Give the extent of all uninfected red blood cells.
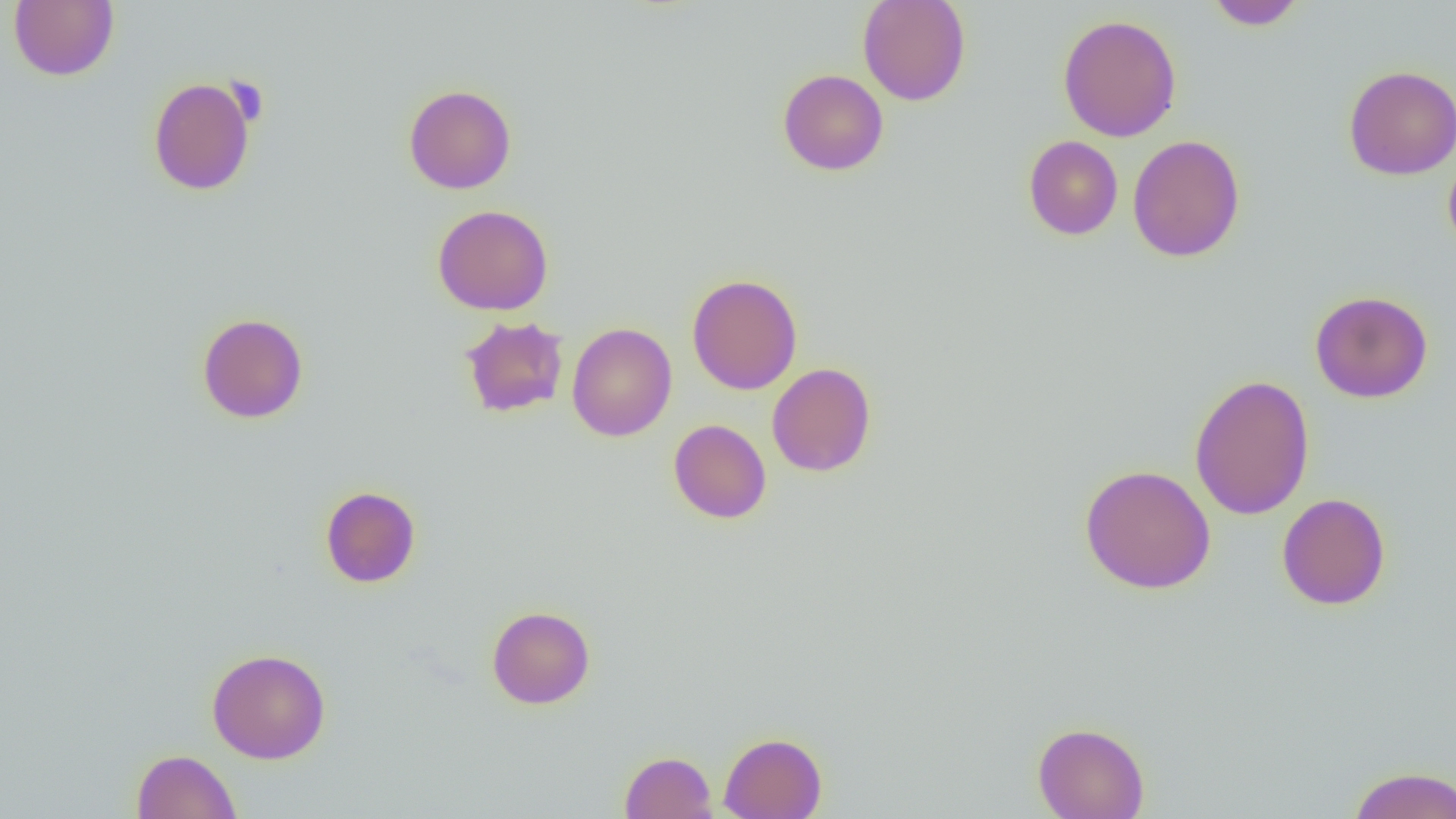
Approximate bounding boxes as (x1, y1, x2, y2) in pixels.
Uninfected red blood cells: (8, 0, 119, 81), (857, 0, 971, 106), (1206, 1, 1306, 30), (1058, 13, 1182, 142), (1342, 65, 1456, 180), (777, 69, 889, 175), (148, 76, 257, 196), (403, 84, 517, 194), (1023, 135, 1123, 240), (1127, 135, 1245, 262), (1443, 150, 1456, 257), (432, 204, 554, 316), (687, 273, 802, 395), (1309, 290, 1433, 404), (197, 313, 308, 423), (460, 316, 569, 418), (566, 322, 677, 442), (767, 363, 877, 477), (1189, 373, 1315, 521), (668, 419, 772, 523), (1079, 464, 1216, 594), (320, 485, 421, 588), (1277, 493, 1390, 610), (486, 605, 595, 709), (207, 648, 331, 764), (1032, 721, 1150, 819), (718, 731, 828, 818), (131, 749, 241, 819), (619, 751, 718, 819), (1346, 766, 1456, 818).

Summary:
  - Slide-level diagnosis: no evidence of blood parasites
  - Image size: 1456×819 pixels
  - Modality: light microscopy
  - Preparation: thin blood film
  - Magnification: 1000x
  - Field of view: one of a larger specimen